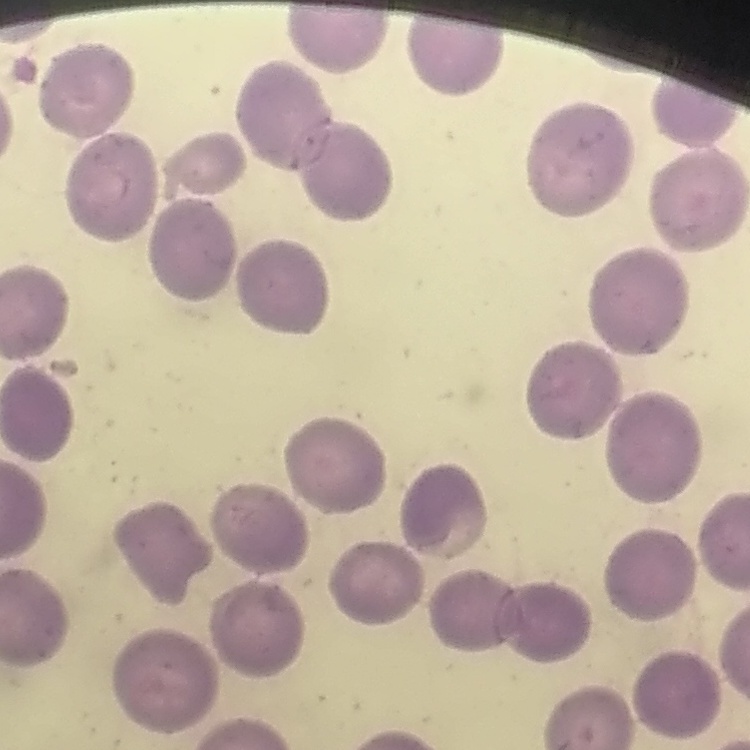

red blood cell morphology = no rouleaux formation
image type = one tile cut from a larger photomicrograph
preparation = thin peripheral smear
stain = Field's or Giemsa